Identify the parasite.
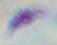

This is Toxoplasma gondii.

Micrograph. 1000x magnification.